Assess for malaria.
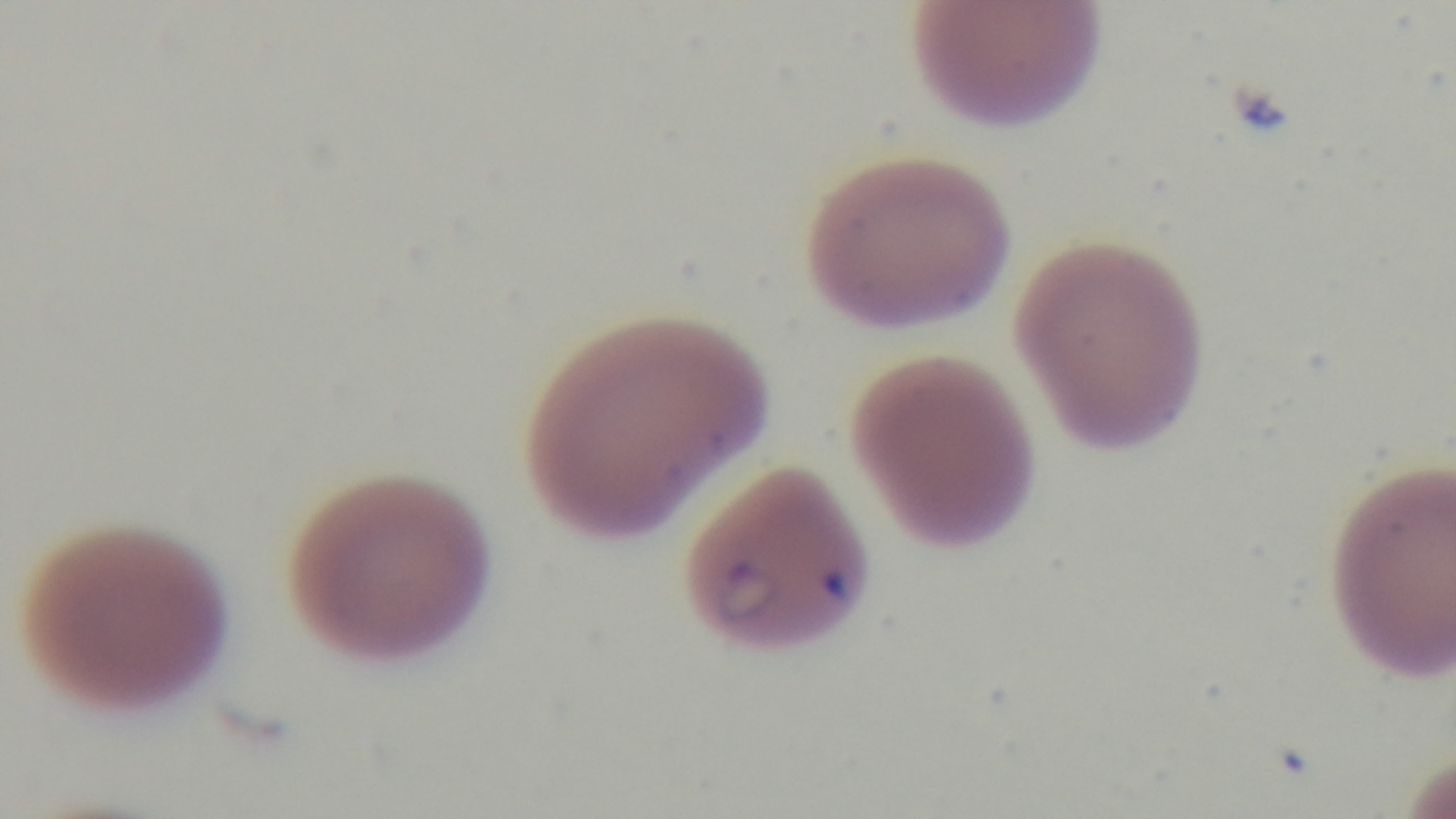
Infected.

Single field of view. Preparation: thin blood film. 100x oil-immersion objective. Light microscopy. Giemsa-stained. Captured with a mounted 4K digital camera.